Point out each malaria parasite.
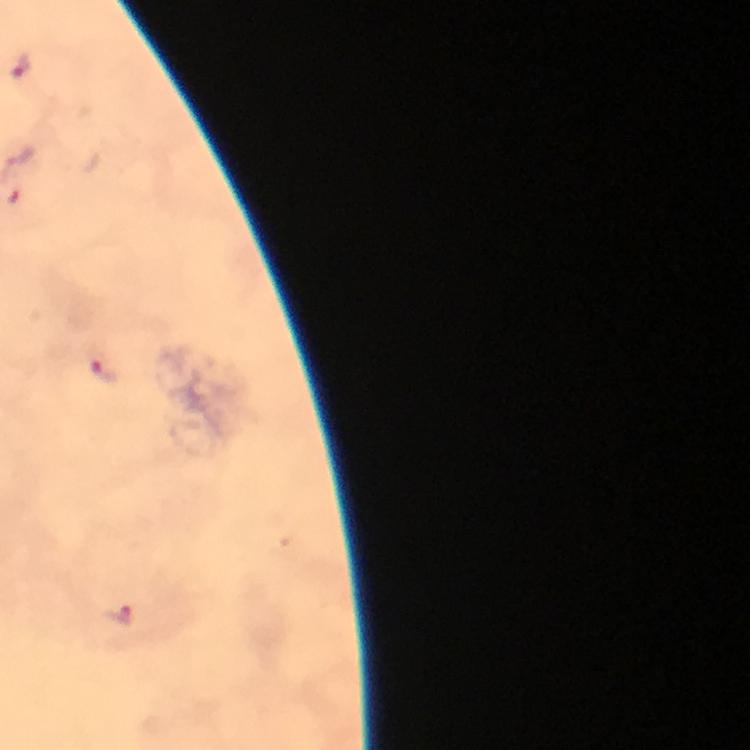

Approximate centers as {x, y} in pixels.
Malaria parasites: {22, 66}, {104, 370}, {122, 617}.

Summary:
  - Context: from a malaria diagnostic workup
  - Preparation: thick smear
  - Magnification: 100x
  - Immersion oil: applied
  - Image size: 750×750 pixels
  - Cropped from: a single field of view
  - Capture: smartphone camera through the microscope
  - Stain: Giemsa